Name the blood parasite species.
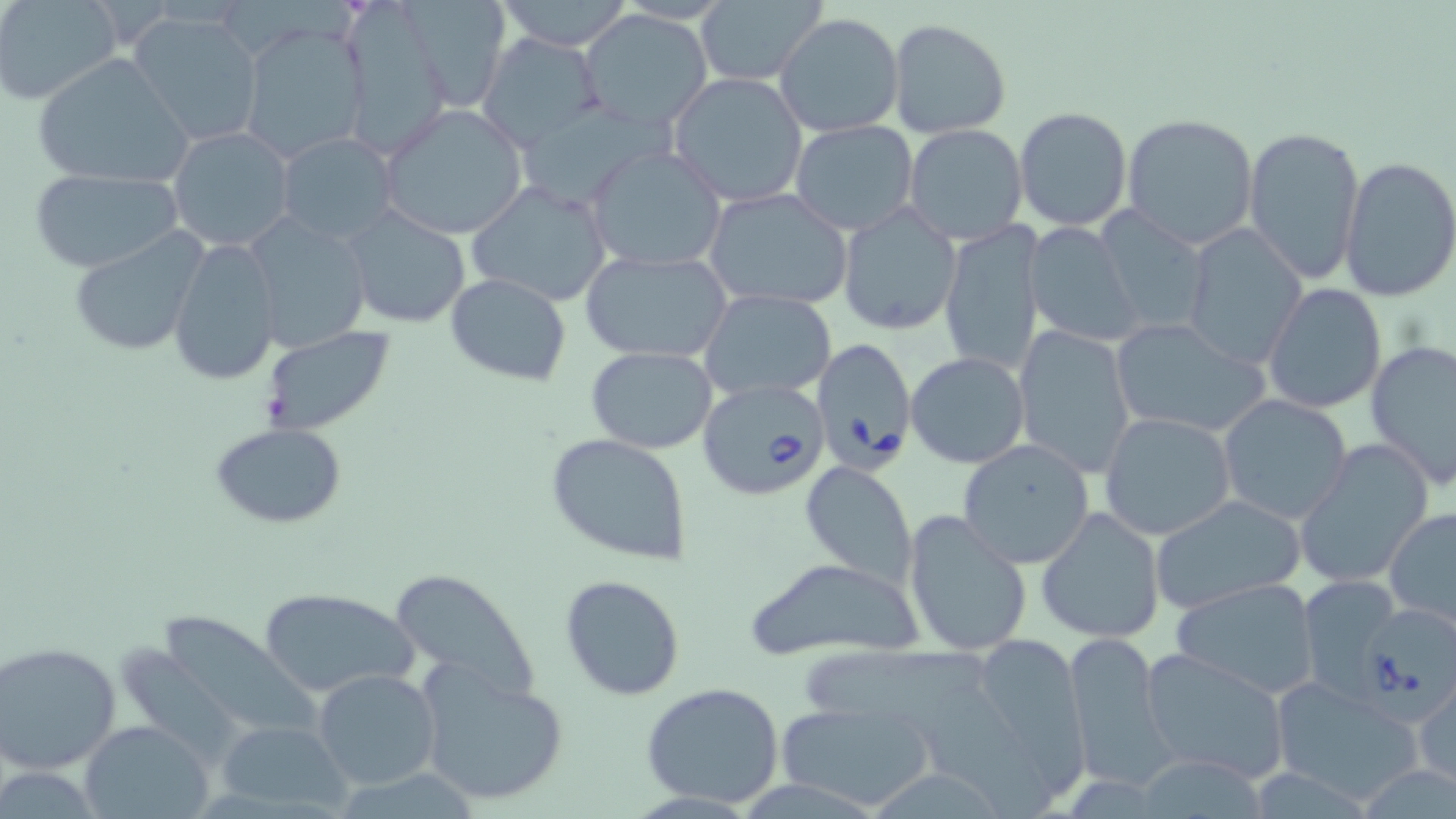

Babesia divergens.

image size = 1456×819 pixels
Babesia divergens-infected red blood cell locations = approximate bounding boxes as [x1, y1, x2, y2] in pixels: [810, 337, 917, 472], [697, 378, 830, 500], [1367, 599, 1456, 721]
modality = optical microscopy
field of view = one of a larger specimen
magnification = 1000x
stain = May-Grünwald-Giemsa
uninfected red blood cell locations = approximate bounding boxes as [x1, y1, x2, y2] in pixels: [2, 0, 122, 105], [401, 0, 512, 111], [495, 0, 637, 51], [691, 3, 827, 86], [579, 9, 711, 131], [352, 11, 454, 151], [129, 12, 264, 148], [774, 13, 905, 137], [887, 18, 1012, 138], [238, 25, 370, 164], [478, 32, 605, 152], [33, 53, 194, 189], [666, 72, 809, 208], [531, 95, 657, 209], [380, 104, 528, 239], [1013, 106, 1134, 231], [1121, 113, 1258, 250], [790, 120, 919, 235], [903, 123, 1030, 247], [1243, 125, 1366, 283], [168, 127, 296, 253], [275, 133, 400, 243], [586, 145, 726, 273], [1340, 156, 1456, 302], [27, 167, 184, 274], [467, 181, 612, 308], [705, 189, 853, 311], [343, 204, 472, 330], [838, 204, 962, 337], [1096, 209, 1211, 336], [242, 212, 373, 355], [938, 221, 1045, 376], [1025, 223, 1145, 346], [1181, 224, 1308, 369], [66, 229, 209, 357], [167, 236, 281, 385], [582, 248, 733, 364], [445, 273, 572, 385], [1263, 282, 1386, 414], [700, 290, 837, 402], [1109, 316, 1269, 437], [1013, 325, 1136, 477], [259, 326, 399, 437], [1365, 340, 1456, 488], [585, 346, 717, 454], [905, 351, 1031, 468], [1218, 396, 1353, 523], [1099, 412, 1239, 542], [208, 422, 348, 528], [546, 433, 693, 566], [958, 438, 1095, 569], [1296, 440, 1434, 588], [800, 460, 918, 586], [1151, 494, 1306, 616], [1385, 507, 1456, 627], [1036, 508, 1165, 645], [903, 509, 1034, 657], [744, 556, 927, 662], [386, 568, 541, 708], [559, 574, 687, 701], [1298, 574, 1404, 696], [1171, 577, 1323, 700], [256, 585, 420, 700], [169, 612, 318, 727], [960, 631, 1090, 782], [1066, 632, 1169, 787], [116, 638, 231, 758], [1, 642, 121, 772], [805, 645, 994, 723], [1140, 649, 1291, 784], [417, 664, 567, 806], [313, 670, 440, 790], [1269, 675, 1423, 803], [641, 682, 785, 808], [1414, 683, 1455, 789], [927, 688, 1059, 818], [776, 701, 935, 810], [80, 720, 211, 819], [215, 720, 350, 813], [1141, 757, 1274, 814]
preparation = thin blood smear